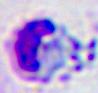 A white blood cell is shown. Micrograph. 400x magnification.